Locate every P. falciparum parasite and give its life-cycle stage, and locate every leukocyte and any debris.
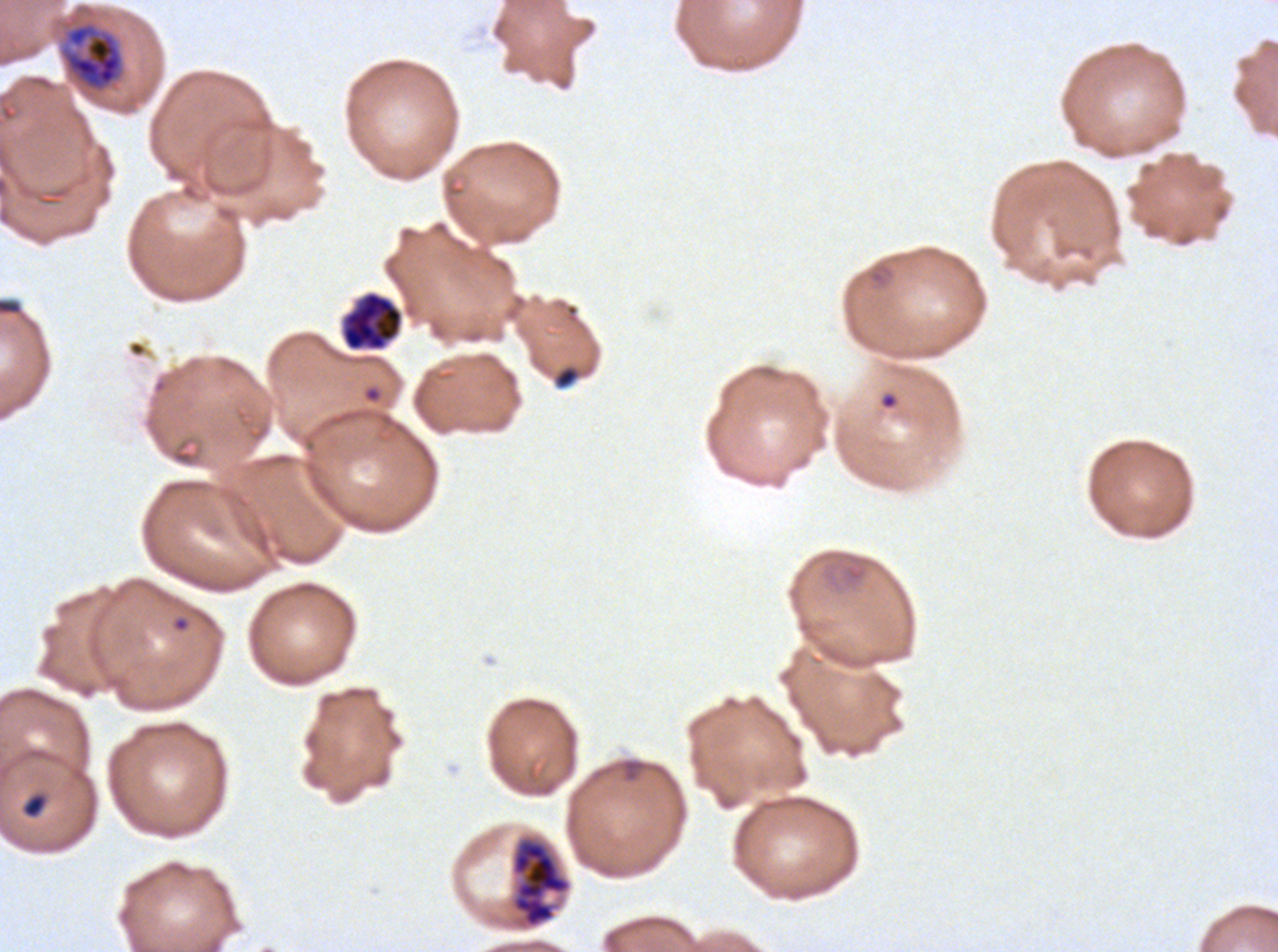

Approximate bounding boxes as [x1, y1, x2, y2] in pixels.
Rings: [866, 262, 895, 288], [362, 384, 383, 404], [879, 390, 900, 411], [821, 551, 872, 591], [170, 615, 191, 634].
Late trophozoites: [58, 20, 125, 93].
Late schizonts: [341, 291, 403, 351], [508, 833, 573, 932].
Debris: [0, 298, 23, 316], [552, 363, 582, 390], [21, 792, 48, 819].
No late-ring/early-trophozoite forms, mid trophozoites, early schizonts, segmenters, gametocytes, or leukocytes observed.

Summary:
  - Stain: Giemsa
  - Life-cycle stages observed: ring, late trophozoite, late schizont
  - Image size: 1278×952 pixels
  - Field of view: one sub-image of a larger composite
  - Preparation: thin blood smear
  - Specimen: P. falciparum from a patient in The Gambia, cultured ex vivo for 24 to 48 hours